Assess the morphology of the erythrocytes.
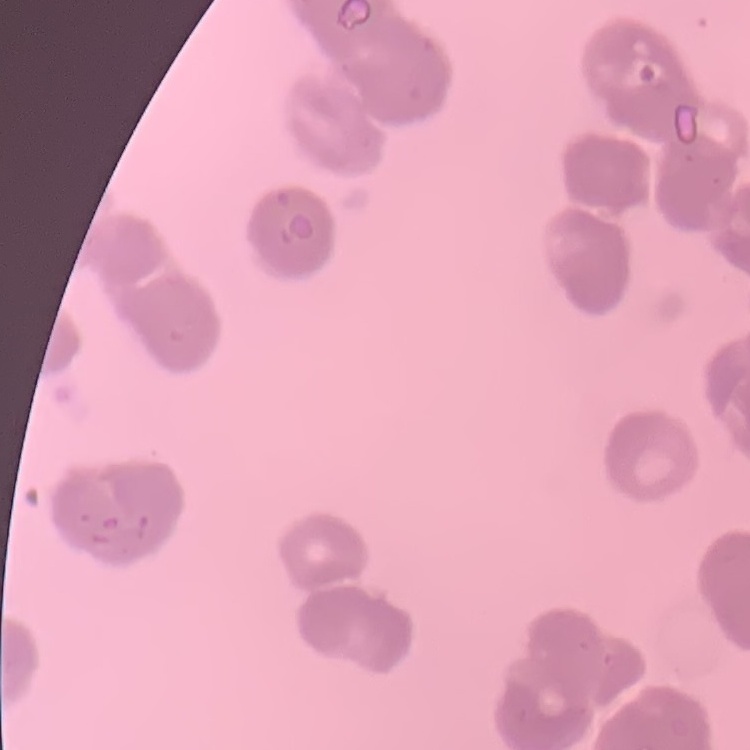

They show rouleaux formation.

stain = Field's or Giemsa
image type = one tile cut from a larger photomicrograph
preparation = thin peripheral smear